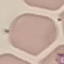

Malaria status: uninfected. Giemsa-stained preparation. Cell patch, automatically extracted from a larger field of view and resized to 64 × 64 pixels. Thin smear of blood. Acquired by smartphone through the microscope eyepiece.